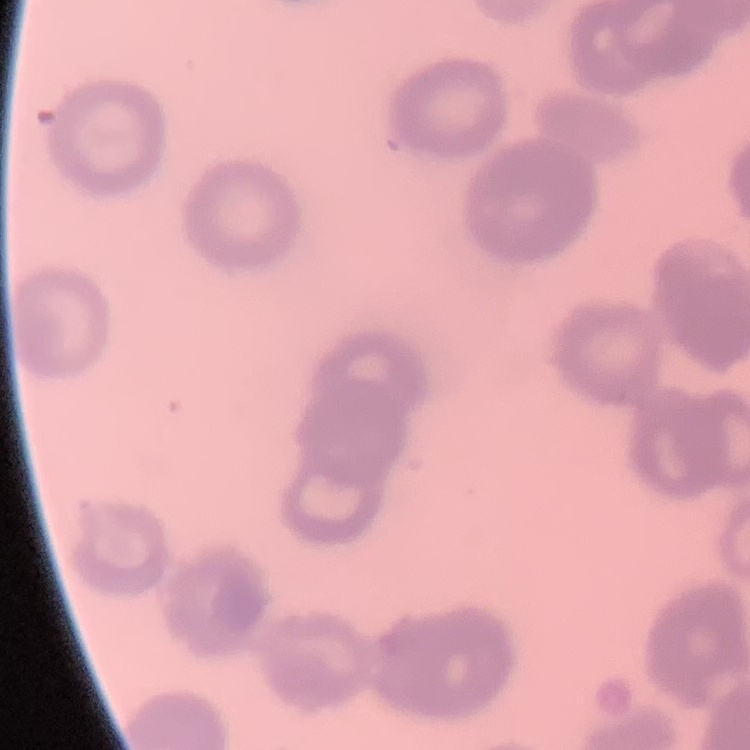
{
  "erythrocyte_morphology": "rouleaux formation",
  "stain": "Field's or Giemsa",
  "preparation": "thin blood film",
  "image_type": "square crop of a larger photomicrograph"
}